Identify the parasite.
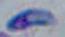

Toxoplasma gondii.

modality: micrograph
magnification: 1000x